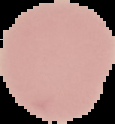 Malaria status: uninfected. From a thin blood film. Image is 115×124 pixels. Segmented cell region on a black background.